Report the malaria status of this cell.
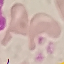

It is uninfected.

{
  "stain": "Giemsa",
  "capture": "smartphone through the microscope eyepiece",
  "image_type": "automatically extracted cell patch, resized to 64 × 64 pixels",
  "preparation": "thin blood film"
}